Locate platelets.
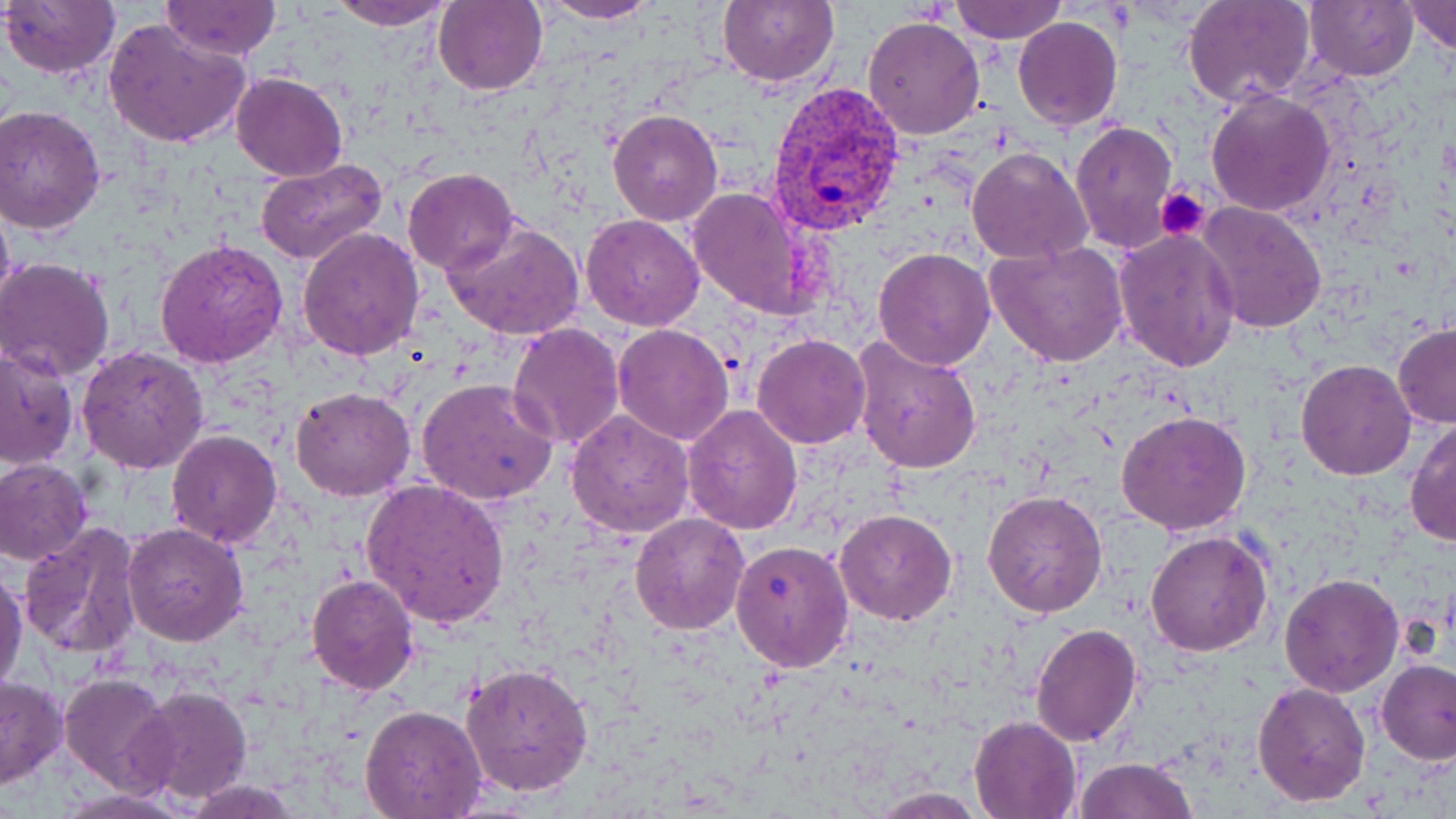
Approximate bounding boxes as named x1/y1/x2/y2 corners in pixels.
Platelets: (x1=1156, y1=186, x2=1211, y2=242).

{
  "slide_level_diagnosis": "Plasmodium vivax",
  "magnification": "1000x",
  "preparation": "thin blood film",
  "plasmodium_vivax_infected_red_blood_cell_locations": "approximate bounding boxes as named x1/y1/x2/y2 corners in pixels: (x1=766, y1=82, x2=907, y2=237)",
  "field_of_view": "one of a larger specimen",
  "image_size": "1456×819 pixels",
  "uninfected_red_blood_cell_locations": "approximate bounding boxes as named x1/y1/x2/y2 corners in pixels: (x1=1, y1=0, x2=121, y2=79), (x1=327, y1=0, x2=457, y2=28), (x1=534, y1=0, x2=662, y2=24), (x1=718, y1=0, x2=838, y2=87), (x1=950, y1=0, x2=1068, y2=44), (x1=1303, y1=0, x2=1417, y2=82), (x1=160, y1=1, x2=283, y2=59), (x1=434, y1=1, x2=548, y2=95), (x1=1185, y1=1, x2=1313, y2=106), (x1=1402, y1=1, x2=1456, y2=54), (x1=862, y1=16, x2=986, y2=139), (x1=1013, y1=16, x2=1123, y2=132), (x1=104, y1=18, x2=251, y2=149), (x1=230, y1=73, x2=347, y2=181), (x1=1204, y1=87, x2=1336, y2=216), (x1=0, y1=105, x2=106, y2=233), (x1=606, y1=108, x2=724, y2=226), (x1=1070, y1=120, x2=1177, y2=252), (x1=966, y1=145, x2=1094, y2=264), (x1=255, y1=159, x2=389, y2=268), (x1=403, y1=168, x2=519, y2=275), (x1=686, y1=187, x2=817, y2=320), (x1=0, y1=189, x2=15, y2=317), (x1=1197, y1=201, x2=1326, y2=335), (x1=581, y1=213, x2=705, y2=329), (x1=443, y1=218, x2=585, y2=340), (x1=296, y1=226, x2=424, y2=360), (x1=1112, y1=228, x2=1241, y2=373), (x1=156, y1=238, x2=291, y2=369), (x1=985, y1=240, x2=1129, y2=368), (x1=872, y1=246, x2=997, y2=370), (x1=0, y1=258, x2=117, y2=379), (x1=508, y1=322, x2=627, y2=451), (x1=1392, y1=322, x2=1455, y2=429), (x1=611, y1=323, x2=736, y2=445), (x1=752, y1=333, x2=870, y2=449), (x1=851, y1=335, x2=983, y2=474), (x1=0, y1=342, x2=78, y2=469), (x1=75, y1=344, x2=209, y2=473), (x1=1295, y1=359, x2=1415, y2=480), (x1=416, y1=378, x2=559, y2=504), (x1=290, y1=386, x2=415, y2=501), (x1=681, y1=404, x2=802, y2=535), (x1=1117, y1=408, x2=1251, y2=535), (x1=565, y1=409, x2=694, y2=537), (x1=1406, y1=417, x2=1456, y2=549), (x1=166, y1=428, x2=282, y2=548), (x1=0, y1=458, x2=92, y2=565), (x1=359, y1=479, x2=511, y2=627), (x1=983, y1=491, x2=1107, y2=618), (x1=834, y1=508, x2=959, y2=625), (x1=629, y1=513, x2=750, y2=634), (x1=123, y1=522, x2=249, y2=646), (x1=19, y1=523, x2=144, y2=664), (x1=1144, y1=531, x2=1273, y2=656), (x1=729, y1=538, x2=856, y2=671), (x1=1, y1=567, x2=26, y2=697), (x1=1279, y1=572, x2=1403, y2=697), (x1=305, y1=573, x2=418, y2=694), (x1=1031, y1=624, x2=1142, y2=747), (x1=1376, y1=659, x2=1456, y2=765), (x1=461, y1=662, x2=594, y2=797), (x1=58, y1=673, x2=175, y2=795), (x1=0, y1=674, x2=67, y2=789), (x1=1253, y1=679, x2=1370, y2=806), (x1=133, y1=685, x2=252, y2=804), (x1=358, y1=703, x2=488, y2=818), (x1=969, y1=714, x2=1082, y2=818), (x1=1075, y1=756, x2=1199, y2=818), (x1=181, y1=778, x2=300, y2=817), (x1=52, y1=787, x2=194, y2=818), (x1=865, y1=788, x2=992, y2=817)",
  "modality": "light microscopy",
  "stain": "May-Grünwald-Giemsa"
}